Mark where platelets are.
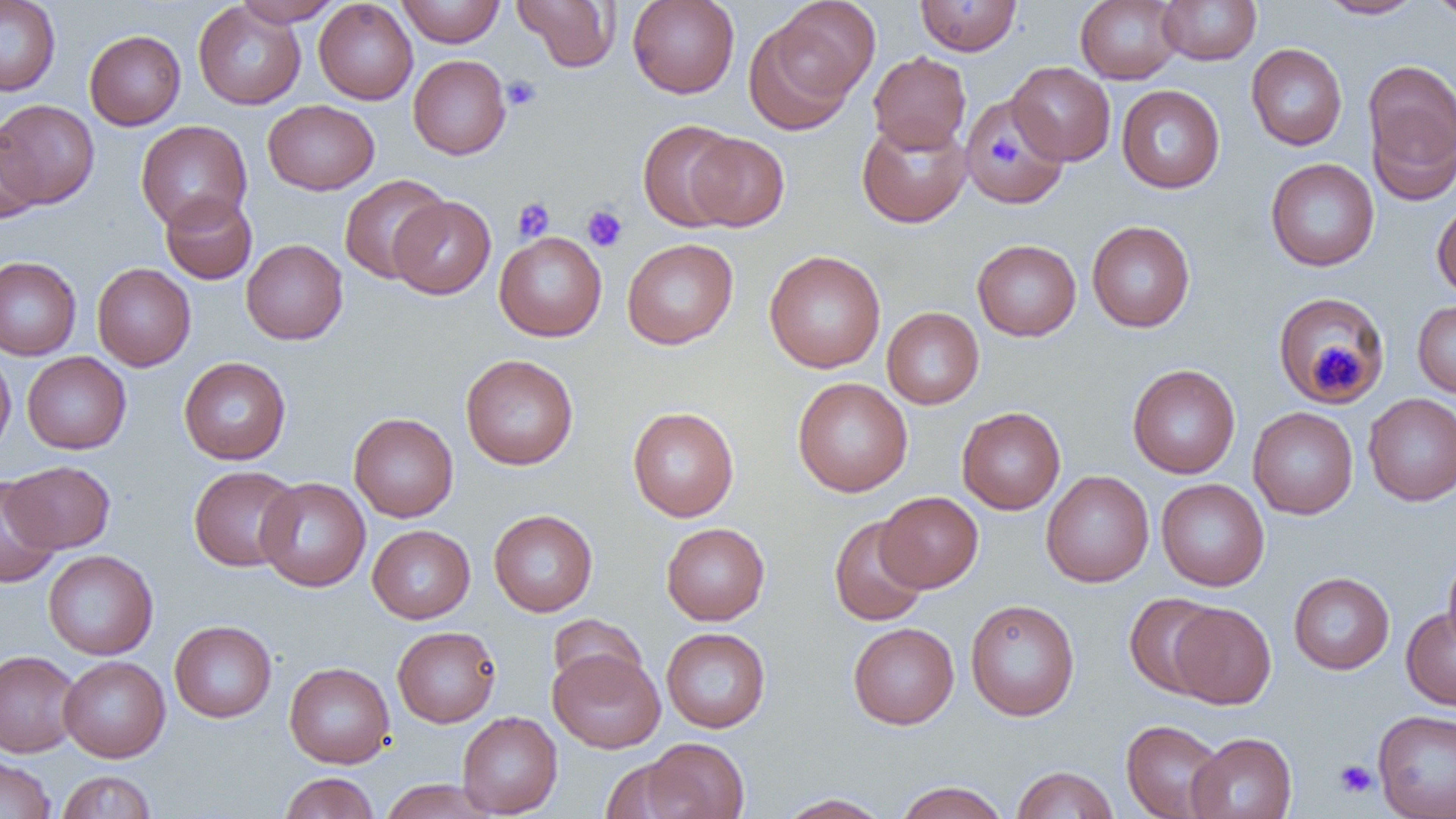

Approximate bounding boxes as [x1, y1, x2, y2] in pixels.
Platelets: [501, 75, 542, 110], [989, 133, 1021, 167], [512, 197, 555, 242], [582, 205, 628, 251], [1313, 342, 1362, 395], [1334, 759, 1377, 798].

Uninfected red blood cell locations: [233, 0, 343, 26], [314, 0, 418, 105], [396, 0, 505, 47], [512, 0, 620, 72], [627, 0, 740, 99], [769, 0, 881, 102], [914, 0, 1022, 56], [1075, 0, 1183, 84], [1157, 0, 1262, 65], [1317, 0, 1424, 19], [1427, 0, 1456, 22], [0, 1, 61, 96], [193, 3, 306, 109], [742, 17, 863, 136], [84, 30, 186, 130], [1246, 43, 1347, 150], [868, 51, 971, 153], [408, 54, 511, 160], [1363, 58, 1456, 199], [1007, 61, 1115, 165], [1116, 85, 1225, 193], [960, 95, 1067, 206], [0, 99, 100, 208], [263, 100, 379, 195], [856, 117, 972, 228], [637, 119, 742, 232], [135, 120, 252, 231], [0, 123, 43, 225], [685, 133, 789, 231], [1265, 158, 1379, 271], [338, 174, 450, 284], [160, 191, 257, 285], [388, 196, 495, 299], [1432, 200, 1456, 300], [1087, 220, 1195, 333], [494, 232, 607, 342], [623, 238, 739, 349], [241, 239, 348, 344], [972, 239, 1082, 341], [764, 250, 886, 373], [0, 256, 82, 361], [92, 263, 196, 371], [1272, 292, 1389, 407], [1412, 301, 1456, 398], [882, 307, 984, 409], [0, 350, 16, 458], [22, 351, 132, 454], [460, 354, 578, 470], [179, 357, 291, 465], [1127, 363, 1240, 478], [792, 377, 912, 497], [1364, 393, 1456, 505], [627, 406, 739, 521], [957, 406, 1066, 514], [1248, 407, 1358, 519], [348, 412, 459, 522], [4, 461, 115, 552], [188, 465, 301, 572], [1041, 470, 1154, 587], [0, 475, 60, 588], [256, 477, 370, 591], [1156, 478, 1269, 591], [876, 491, 983, 592], [488, 509, 598, 616], [828, 516, 930, 626], [368, 521, 600, 619], [661, 522, 770, 625], [367, 525, 475, 623], [43, 550, 158, 660], [1442, 550, 1456, 656], [1289, 572, 1395, 674], [1124, 593, 1225, 698], [965, 598, 1080, 721], [1169, 602, 1276, 709], [1401, 607, 1456, 710], [547, 613, 647, 696], [169, 620, 277, 722], [848, 622, 959, 729], [392, 625, 501, 727], [660, 627, 771, 732], [548, 648, 665, 753], [0, 650, 82, 757], [59, 656, 170, 762], [284, 661, 395, 768], [1372, 709, 1456, 819], [457, 711, 563, 818], [1121, 719, 1227, 819], [1187, 732, 1297, 819], [640, 737, 750, 819], [0, 756, 56, 819], [599, 758, 694, 819], [1011, 765, 1118, 819], [57, 770, 158, 819], [279, 772, 379, 818], [378, 779, 497, 819], [894, 781, 1010, 819], [777, 793, 893, 818]. Slide-level diagnosis: no evidence of blood parasites. Thin blood film. Optical microscopy. Image is 1456×819 pixels. Single field of view. Captured at 1000x magnification.